State which parasite is depicted.
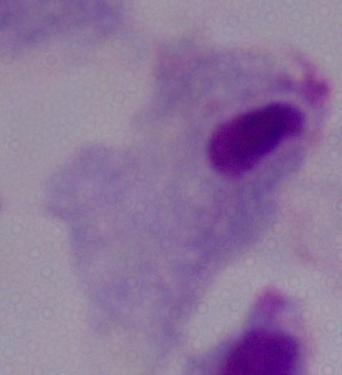

This is a trichomonad.

1000x magnification. Micrograph.